Locate and identify every blood parasite.
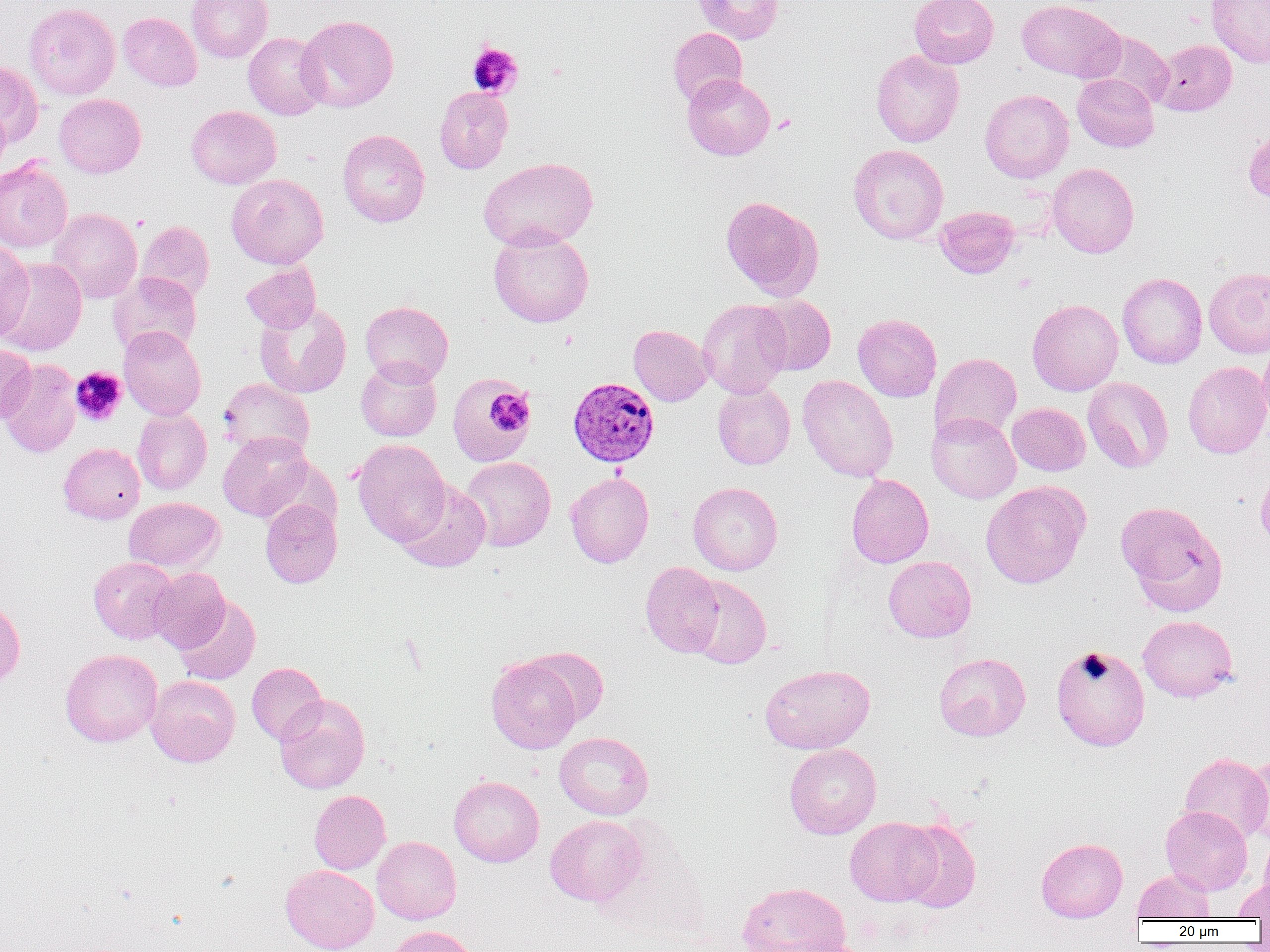
Approximate bounding boxes as (x1,y1)-(x2,y2) corner pairs in pixels.
Plasmodium vivax-infected red blood cells: (568,377)-(660,466).
No Plasmodium falciparum, Plasmodium ovale, Plasmodium malariae, Babesia divergens, or Trypanosoma brucei observed.

{
  "slide_level_diagnosis": "Plasmodium vivax",
  "field_of_view": "one of a larger specimen",
  "magnification": "1000x",
  "image_size": "1270×952 pixels",
  "preparation": "thin blood smear",
  "platelet_locations": "approximate bounding boxes as (x1,y1)-(x2,y2) corner pairs in pixels: (466,41)-(523,99), (772,114)-(797,134), (70,367)-(127,426), (488,390)-(533,435)",
  "modality": "optical microscopy",
  "uninfected_red_blood_cell_locations": "approximate bounding boxes as (x1,y1)-(x2,y2) corner pairs in pixels: (186,0)-(273,63), (691,0)-(784,44), (909,0)-(998,68), (1016,0)-(1122,82), (1206,1)-(1270,67), (24,2)-(121,100), (118,12)-(202,91), (297,15)-(399,112), (668,27)-(747,107), (1088,30)-(1173,109), (243,32)-(329,120), (1152,39)-(1236,116), (870,50)-(964,147), (0,62)-(43,147), (1072,73)-(1159,152), (682,74)-(775,160), (434,87)-(513,174), (980,89)-(1074,182), (54,94)-(146,178), (0,104)-(11,179), (185,105)-(281,189), (1242,128)-(1270,204), (337,129)-(430,227), (848,144)-(948,244), (0,157)-(72,254), (478,157)-(598,251), (1047,163)-(1140,257), (227,174)-(328,269), (720,196)-(823,300), (934,205)-(1020,278), (47,207)-(143,303), (136,220)-(214,303), (488,228)-(594,327), (0,241)-(34,343), (0,258)-(87,356), (241,262)-(321,332), (1204,267)-(1270,358), (108,272)-(202,358), (1117,273)-(1207,369), (754,294)-(836,375), (697,299)-(792,398), (1027,299)-(1123,395), (361,301)-(454,386), (254,302)-(352,398), (853,314)-(942,402), (628,324)-(713,406), (118,327)-(206,420), (1258,340)-(1270,430), (0,344)-(36,424), (929,352)-(1022,443), (0,358)-(81,458), (355,358)-(442,441), (1183,361)-(1270,458), (448,373)-(534,466), (797,374)-(898,482), (1083,376)-(1173,472), (218,378)-(314,459), (712,382)-(795,469), (1007,403)-(1090,476), (132,408)-(212,495), (926,412)-(1021,503), (218,432)-(313,521), (352,439)-(451,547), (59,443)-(145,523), (459,456)-(556,552), (1256,462)-(1270,552), (565,472)-(654,567), (847,474)-(933,568), (396,480)-(491,572), (980,480)-(1091,589), (688,482)-(783,575), (124,497)-(224,574), (260,497)-(342,588), (1115,501)-(1227,614), (88,556)-(179,644), (883,556)-(976,642), (640,562)-(724,657), (148,568)-(230,653), (685,575)-(772,669), (174,595)-(260,686), (0,597)-(25,688), (1138,615)-(1237,702), (1051,644)-(1150,751), (524,647)-(609,726), (59,649)-(163,747), (933,653)-(1031,741), (486,656)-(581,753), (246,662)-(327,745), (760,663)-(875,754), (146,675)-(240,767), (274,695)-(370,794), (554,732)-(654,820), (784,743)-(882,839), (1245,751)-(1270,846), (1179,753)-(1270,843), (449,775)-(544,867), (309,790)-(390,874), (1160,805)-(1252,895), (545,815)-(646,905), (845,817)-(943,906), (900,819)-(981,912), (1259,831)-(1270,906), (372,836)-(461,924), (1036,837)-(1127,922), (280,865)-(379,952), (1132,869)-(1215,921), (1234,877)-(1270,920), (737,881)-(851,952), (386,925)-(478,952), (778,938)-(873,952)"
}